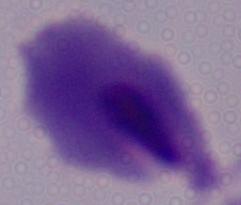
Summary:
  - Modality: micrograph
  - Identification: trichomonad
  - Magnification: 1000x